Point out each leukocyte.
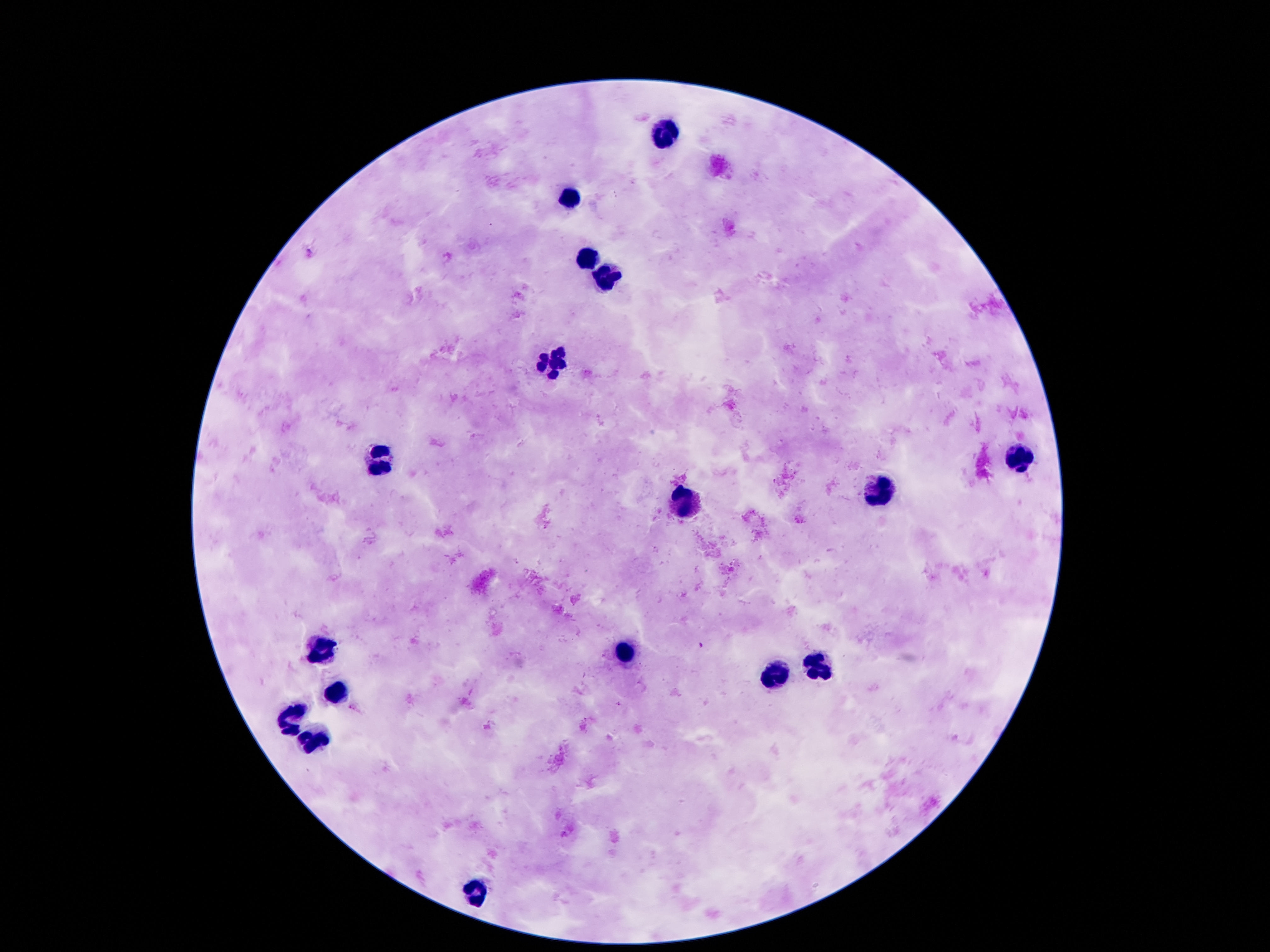

Approximate centers as [x, y] in pixels.
Leukocytes: [666, 135], [567, 198], [586, 259], [603, 279], [554, 363], [1019, 457], [381, 458], [880, 492], [685, 502], [324, 652], [624, 654], [816, 667], [776, 676], [337, 692], [292, 721], [310, 741], [480, 892].

{
  "image_size": "1270×952 pixels",
  "preparation": "thick blood film",
  "magnification": "100x",
  "field_of_view": "one from this slide",
  "capture": "smartphone camera through the microscope eyepiece",
  "patient_malaria_status": "uninfected",
  "stain": "Giemsa"
}